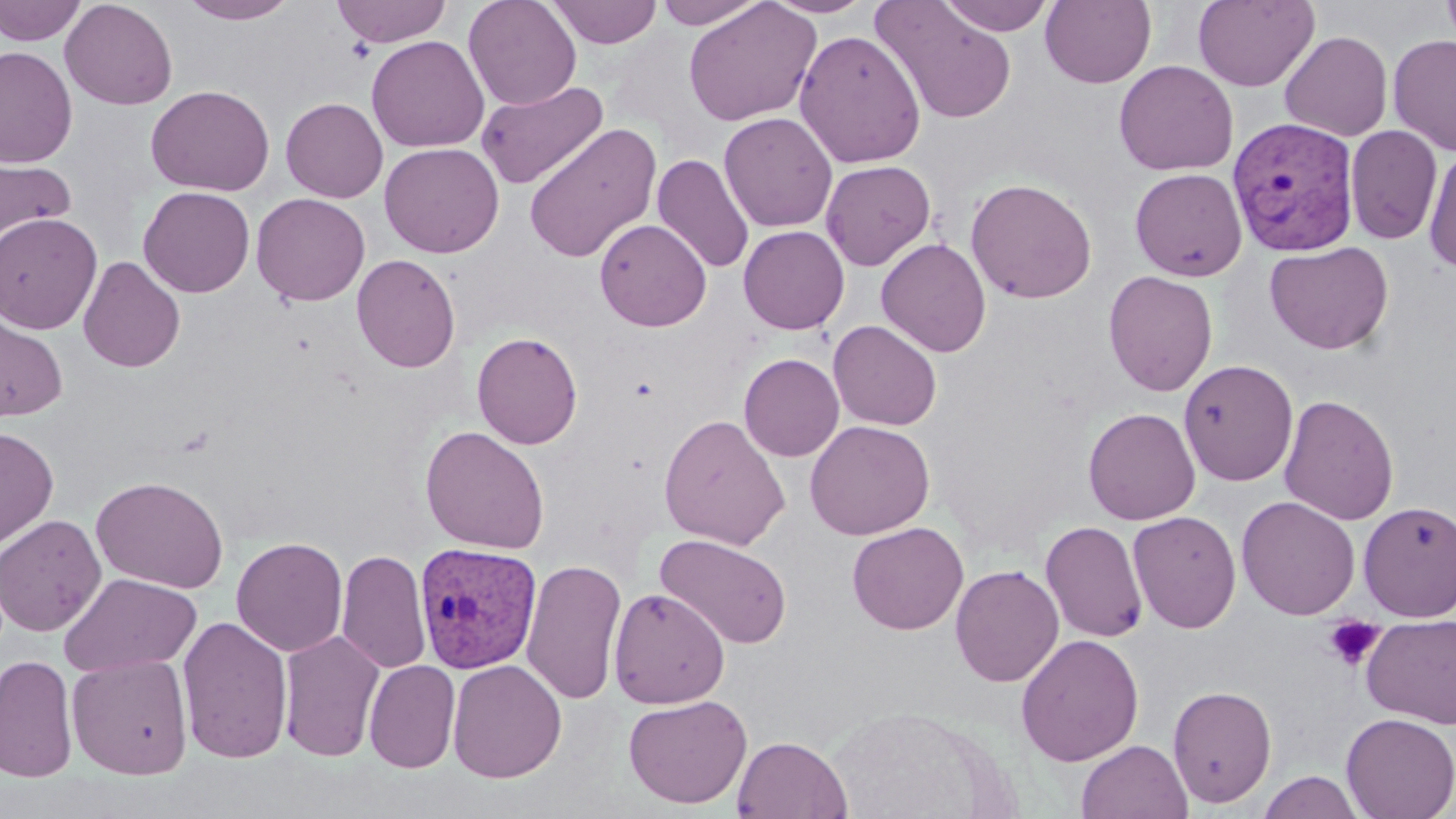

Summary:
  - Coordinate format: approximate bounding boxes as (x1, y1, x2, y2) in pixels
  - Platelet locations: (1322, 616, 1386, 671)
  - Uninfected red blood cell locations: (0, 0, 87, 46), (59, 0, 178, 110), (179, 0, 299, 24), (331, 0, 453, 47), (463, 0, 581, 110), (546, 0, 663, 48), (652, 0, 768, 29), (764, 0, 878, 19), (938, 0, 1058, 36), (1040, 0, 1157, 88), (1193, 0, 1320, 92), (1439, 0, 1456, 50), (683, 1, 821, 126), (871, 1, 1017, 125), (793, 29, 926, 168), (1280, 30, 1393, 141), (1388, 34, 1456, 156), (366, 35, 489, 153), (0, 45, 77, 169), (1114, 60, 1239, 176), (475, 80, 609, 190), (146, 84, 275, 196), (280, 97, 388, 203), (719, 112, 838, 232), (524, 121, 662, 264), (1344, 125, 1443, 245), (379, 142, 504, 257), (1423, 144, 1456, 274), (0, 150, 76, 254), (652, 153, 755, 275), (821, 159, 936, 271), (1129, 168, 1247, 281), (965, 177, 1098, 304), (138, 185, 255, 297), (251, 192, 370, 306), (0, 212, 103, 334), (594, 219, 711, 331), (738, 225, 849, 334), (876, 238, 991, 357), (1264, 241, 1393, 355), (351, 253, 461, 373), (78, 255, 186, 373), (1103, 270, 1218, 397), (0, 309, 68, 422), (828, 320, 942, 430), (471, 331, 583, 449), (735, 345, 943, 451), (739, 353, 844, 461), (1179, 359, 1299, 487), (1279, 393, 1399, 526), (1082, 407, 1201, 525), (658, 414, 791, 550), (805, 420, 935, 540), (420, 425, 551, 554), (0, 426, 59, 550), (90, 475, 230, 593), (1236, 496, 1360, 620), (1358, 500, 1456, 622), (1128, 510, 1242, 634), (0, 514, 107, 636), (1040, 520, 1148, 643), (847, 522, 968, 635), (655, 533, 793, 650), (231, 536, 348, 657), (336, 549, 432, 674), (520, 557, 627, 705), (950, 564, 1065, 687), (59, 572, 201, 678), (608, 588, 730, 708), (1361, 614, 1456, 729), (177, 615, 293, 764), (278, 630, 386, 762), (1016, 633, 1144, 766), (0, 653, 78, 783), (67, 653, 193, 780), (447, 659, 567, 783), (364, 660, 461, 773), (1168, 683, 1277, 808), (622, 694, 753, 809), (823, 707, 1012, 819), (1341, 713, 1456, 819), (733, 736, 852, 819), (1076, 739, 1192, 819), (1256, 770, 1366, 819)
  - Plasmodium vivax-infected red blood cell locations: (1226, 115, 1360, 255), (415, 541, 542, 674)
  - Slide-level diagnosis: Plasmodium vivax
  - Stain: May-Grünwald-Giemsa
  - Magnification: 1000x
  - Field of view: one of a larger specimen
  - Image size: 1456×819 pixels
  - Modality: optical microscopy
  - Preparation: thin blood film